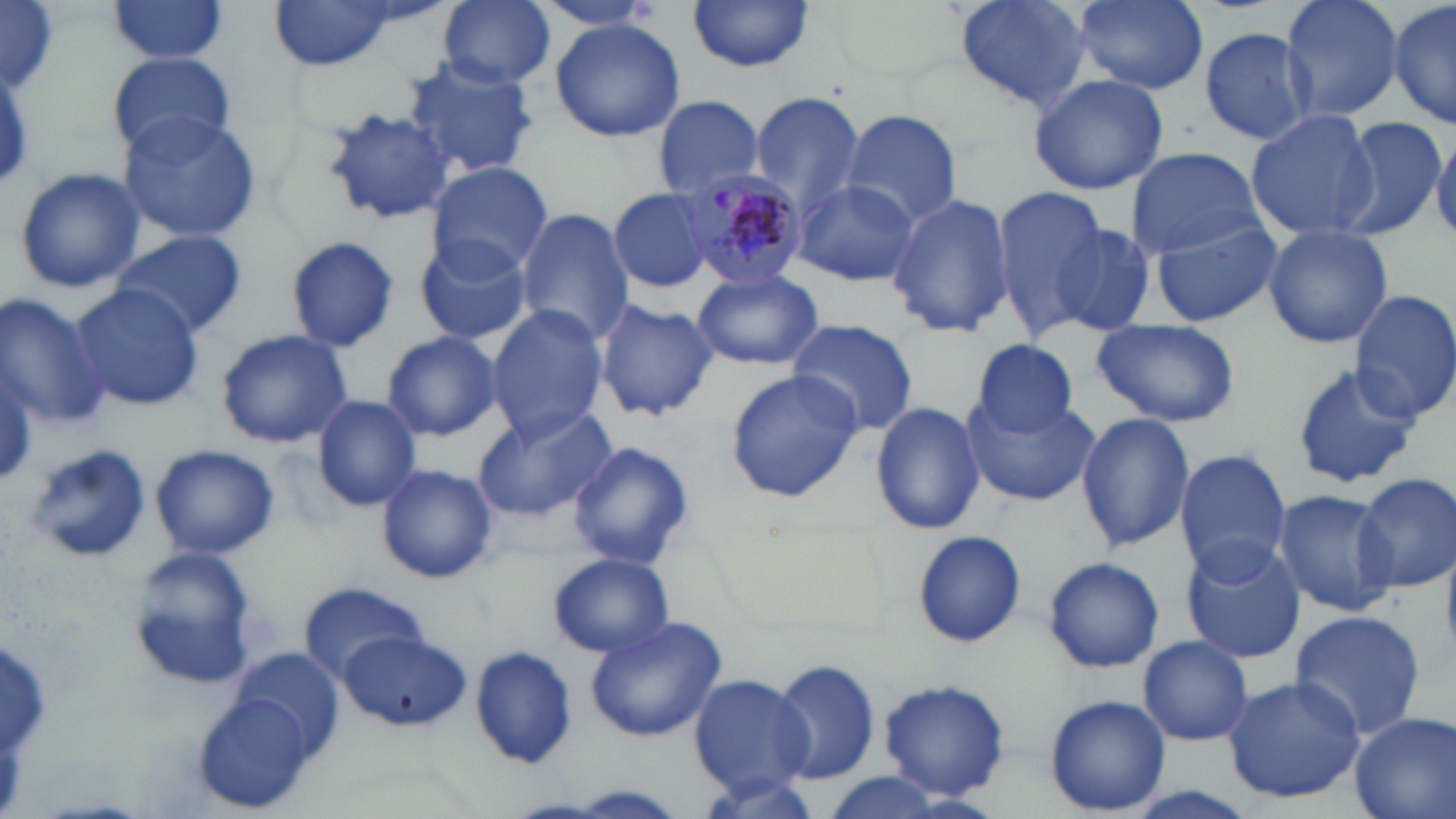
Summary:
  - Coordinate format: approximate bounding boxes as [x1, y1, x2, y2] in pixels
  - Plasmodium malariae-infected red blood cell locations: [680, 166, 808, 283]
  - Uninfected red blood cell locations: [1, 0, 59, 93], [440, 0, 555, 89], [952, 0, 1091, 112], [1073, 0, 1207, 93], [1279, 0, 1403, 125], [1389, 0, 1454, 132], [105, 1, 230, 64], [533, 1, 665, 34], [688, 1, 815, 74], [269, 3, 400, 70], [549, 20, 686, 143], [1200, 25, 1316, 145], [108, 51, 237, 158], [400, 56, 542, 178], [1028, 72, 1169, 195], [748, 91, 866, 214], [652, 96, 765, 198], [323, 108, 453, 224], [1246, 108, 1384, 241], [840, 110, 963, 228], [113, 113, 264, 242], [1337, 117, 1448, 241], [1430, 131, 1456, 239], [1125, 146, 1264, 259], [424, 161, 552, 278], [12, 165, 147, 295], [792, 177, 921, 287], [990, 185, 1105, 331], [607, 187, 715, 295], [886, 192, 1016, 340], [515, 208, 633, 346], [1148, 214, 1282, 328], [1043, 220, 1160, 339], [1261, 224, 1392, 350], [109, 230, 246, 338], [414, 234, 532, 346], [285, 235, 400, 351], [691, 267, 825, 370], [71, 282, 203, 411], [1349, 287, 1456, 424], [1, 291, 110, 432], [594, 299, 718, 421], [485, 304, 609, 440], [1089, 318, 1242, 427], [786, 319, 919, 436], [215, 327, 352, 448], [380, 331, 504, 441], [967, 337, 1084, 438], [1290, 361, 1420, 490], [725, 371, 864, 501], [311, 395, 423, 512], [962, 395, 1098, 506], [870, 401, 987, 536], [471, 403, 619, 521], [1076, 413, 1195, 553], [17, 442, 150, 564], [569, 442, 694, 570], [151, 443, 280, 560], [1173, 448, 1291, 579], [375, 463, 498, 584], [1355, 473, 1456, 593], [1271, 490, 1398, 617], [913, 530, 1026, 648], [1181, 538, 1307, 662], [127, 546, 261, 692], [549, 553, 674, 657], [1043, 557, 1164, 673], [297, 581, 428, 683], [1286, 609, 1428, 742], [585, 614, 728, 743], [340, 631, 470, 731], [1137, 636, 1252, 746], [471, 646, 576, 767], [768, 657, 882, 787], [689, 673, 812, 794], [1222, 674, 1365, 805], [875, 677, 1010, 801], [188, 687, 324, 813], [1044, 695, 1170, 815], [1348, 712, 1455, 819], [692, 771, 818, 818], [819, 772, 950, 819]
  - Slide-level diagnosis: Plasmodium malariae
  - Magnification: 1000x
  - Modality: light microscopy
  - Field of view: one of a larger specimen
  - Preparation: thin blood film
  - Image size: 1456×819 pixels
  - Stain: May-Grünwald-Giemsa